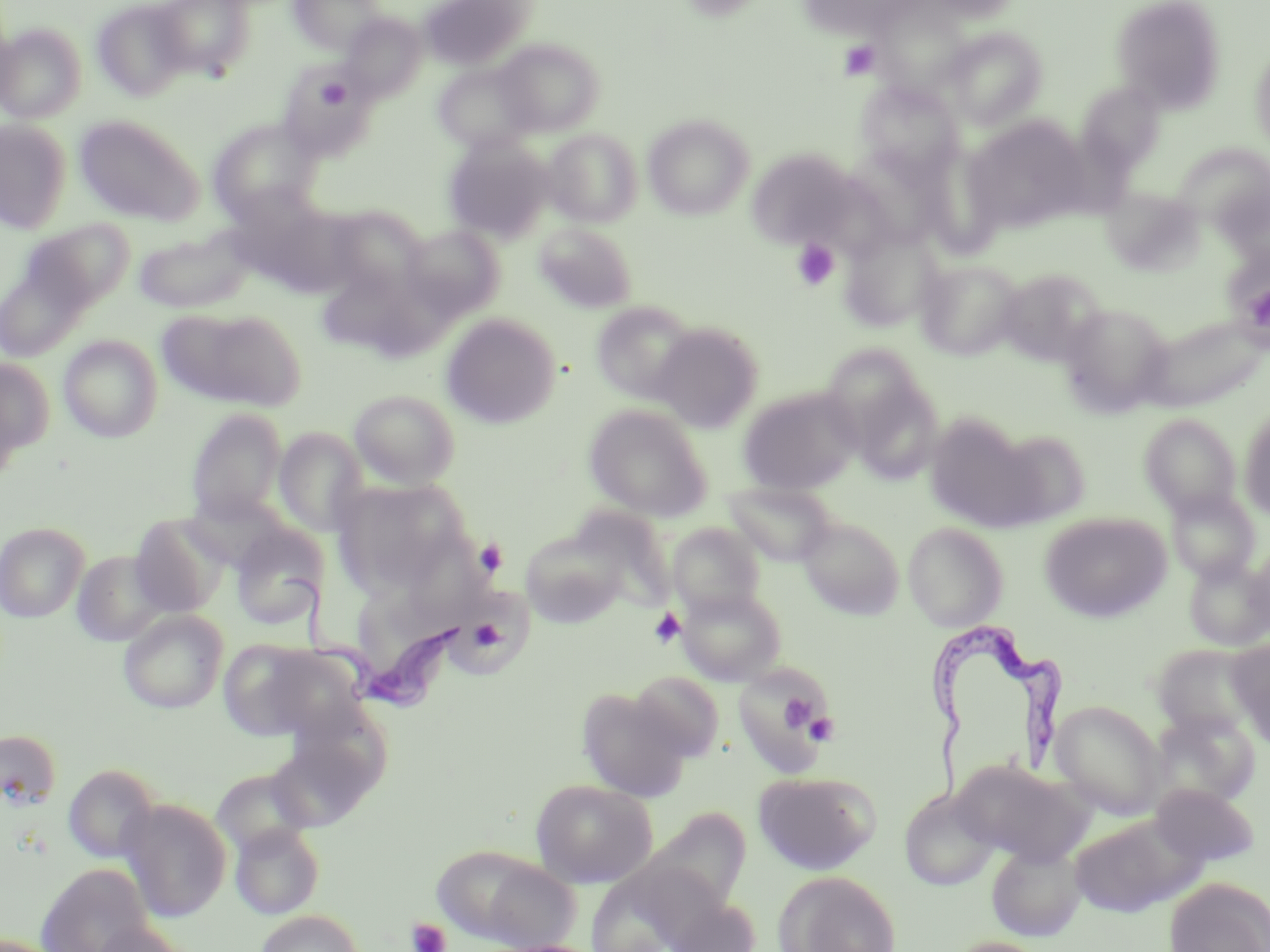

slide-level diagnosis = Trypanosoma brucei
platelet locations = approximate bounding boxes as (x1, y1, x2, y2) in pixels: (838, 40, 880, 80), (318, 77, 350, 108), (792, 238, 840, 290), (1245, 284, 1270, 335), (474, 539, 509, 577), (649, 608, 686, 648), (465, 616, 507, 653), (770, 690, 822, 737), (803, 711, 840, 746), (407, 917, 451, 952)
uninfected red blood cell locations = approximate bounding boxes as (x1, y1, x2, y2) in pixels: (152, 0, 255, 78), (289, 0, 386, 53), (418, 0, 536, 71), (797, 0, 917, 37), (1111, 0, 1227, 113), (92, 1, 193, 100), (340, 13, 426, 101), (0, 23, 87, 123), (944, 27, 1047, 129), (495, 38, 605, 136), (1249, 46, 1270, 152), (433, 62, 538, 154), (857, 80, 966, 183), (1076, 81, 1165, 173), (74, 115, 204, 226), (643, 115, 754, 220), (962, 117, 1094, 235), (0, 119, 72, 232), (208, 119, 320, 223), (542, 129, 642, 226), (443, 136, 555, 242), (1172, 144, 1270, 233), (747, 147, 858, 248), (1102, 186, 1205, 274), (322, 205, 428, 299), (21, 219, 135, 316), (534, 222, 637, 313), (403, 225, 504, 321), (839, 225, 946, 332), (134, 227, 254, 313), (0, 258, 95, 363), (915, 259, 1023, 360), (315, 264, 420, 357), (997, 268, 1105, 366), (590, 301, 698, 403), (1059, 303, 1173, 415), (160, 306, 305, 411), (441, 313, 561, 429), (1142, 315, 1268, 413), (652, 322, 764, 432), (58, 335, 163, 442), (827, 353, 942, 480), (0, 357, 55, 460), (739, 386, 863, 495), (349, 389, 460, 489), (583, 404, 713, 521), (1239, 406, 1270, 520), (186, 408, 287, 523), (1140, 413, 1242, 517), (925, 416, 1043, 531), (274, 427, 369, 537), (994, 430, 1092, 526), (333, 480, 467, 595), (723, 480, 837, 567), (1166, 487, 1260, 583), (567, 507, 676, 608), (1039, 512, 1172, 623), (130, 514, 231, 618), (797, 514, 904, 620), (903, 521, 1009, 631), (0, 522, 89, 623), (667, 522, 767, 617), (230, 524, 329, 630), (520, 529, 628, 628), (1244, 542, 1270, 635), (71, 549, 173, 647), (1183, 556, 1270, 652), (347, 567, 467, 695), (677, 586, 786, 685), (455, 589, 534, 677), (118, 609, 227, 713), (220, 638, 363, 742), (1229, 638, 1270, 745), (1151, 644, 1261, 738), (732, 664, 837, 778), (630, 671, 724, 762), (576, 688, 692, 801), (1050, 701, 1166, 818), (1150, 710, 1260, 808), (265, 728, 381, 831), (0, 729, 62, 811), (954, 760, 1088, 866), (63, 764, 159, 864), (210, 767, 316, 859), (753, 770, 880, 875), (531, 779, 658, 887), (1152, 783, 1260, 868), (899, 787, 999, 891), (118, 798, 232, 923), (643, 808, 751, 911), (1069, 813, 1201, 918), (230, 822, 325, 920), (986, 841, 1087, 941), (432, 845, 581, 950), (35, 863, 150, 952), (775, 871, 900, 952), (1164, 877, 1270, 952), (665, 899, 761, 952), (254, 909, 365, 951), (90, 921, 195, 952), (944, 936, 1052, 952)
magnification = 1000x
stain = May-Grünwald-Giemsa
modality = optical microscopy
Trypanosoma brucei locations = approximate bounding boxes as (x1, y1, x2, y2) in pixels: (268, 568, 472, 711), (919, 616, 1065, 811)
preparation = thin blood film
image size = 1270×952 pixels
field of view = single